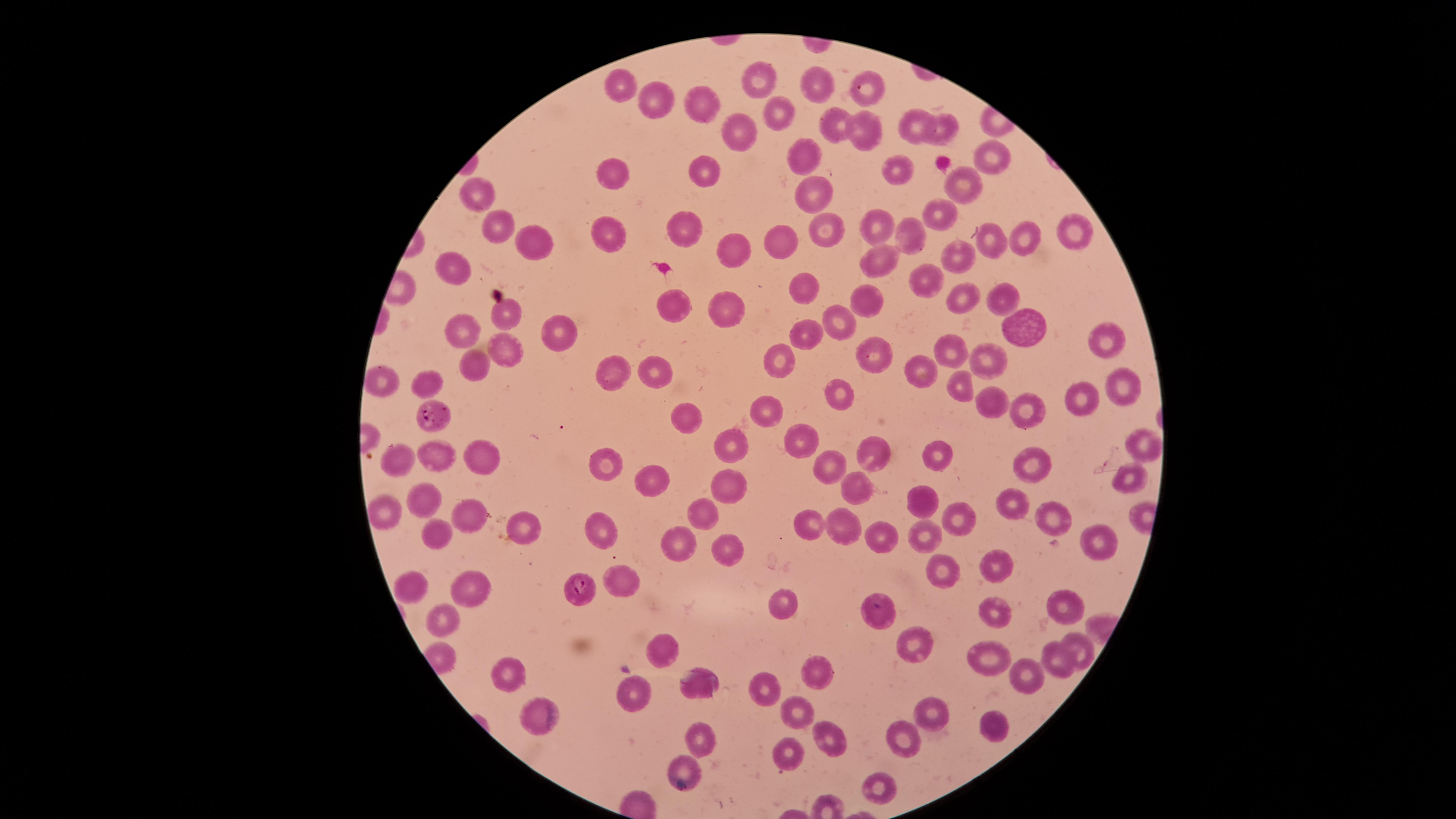 Approximate marker points as [x, y] in pixels. Uninfected red blood cells: [763, 79], [818, 79], [629, 85], [655, 98], [702, 101], [775, 109], [829, 121], [918, 125], [941, 125], [858, 127], [740, 132], [803, 155], [988, 156], [696, 162], [895, 167], [613, 175], [961, 184], [811, 191], [477, 194], [940, 209], [874, 223], [825, 226], [503, 227], [682, 228], [1080, 228], [916, 235], [615, 236], [1029, 237], [536, 238], [782, 239], [995, 243], [727, 252], [958, 255], [880, 259], [459, 265], [920, 276], [802, 286], [864, 297], [1003, 299], [964, 300], [725, 306], [679, 308], [498, 310], [840, 323], [1019, 323], [461, 326], [810, 330], [552, 331], [1106, 338], [507, 345], [946, 348], [871, 352], [989, 354], [788, 362], [605, 367], [477, 368], [650, 372], [913, 373], [387, 381], [423, 381], [959, 383], [1122, 383], [1083, 394], [847, 400], [992, 402], [1029, 404], [774, 405], [685, 411], [806, 439], [733, 440], [1139, 443], [873, 449], [933, 451], [480, 455], [443, 456], [403, 458], [614, 460], [1036, 464], [833, 467], [657, 475], [733, 479], [1123, 479], [853, 485], [924, 494], [428, 499], [1015, 499], [706, 504], [385, 509], [470, 514], [1045, 516], [954, 518], [842, 521], [808, 524], [521, 528], [598, 528], [441, 532], [680, 532], [882, 532], [927, 535], [1095, 535], [726, 548], [1002, 556], [941, 566], [621, 577], [416, 583], [464, 584], [1067, 599], [788, 602], [999, 607], [444, 614], [879, 615], [669, 644], [913, 645], [1081, 645], [985, 654], [1054, 656], [816, 669], [511, 671], [1032, 676], [695, 680], [765, 684], [645, 697], [794, 703], [534, 708], [931, 709], [999, 729], [702, 734], [834, 736], [902, 739], [787, 757], [687, 764], [880, 784]. Parasitized red blood cells: [432, 415], [578, 587]. The visible region is circular. Smartphone photograph through the microscope eyepiece. Species: Plasmodium falciparum. Image is 1456×819 pixels. Presence: malaria parasites detected. Giemsa stain. Single field of view. Thin blood smear.